Identify the parasite.
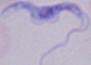

A trypanosome.

Micrograph. 1000x magnification.